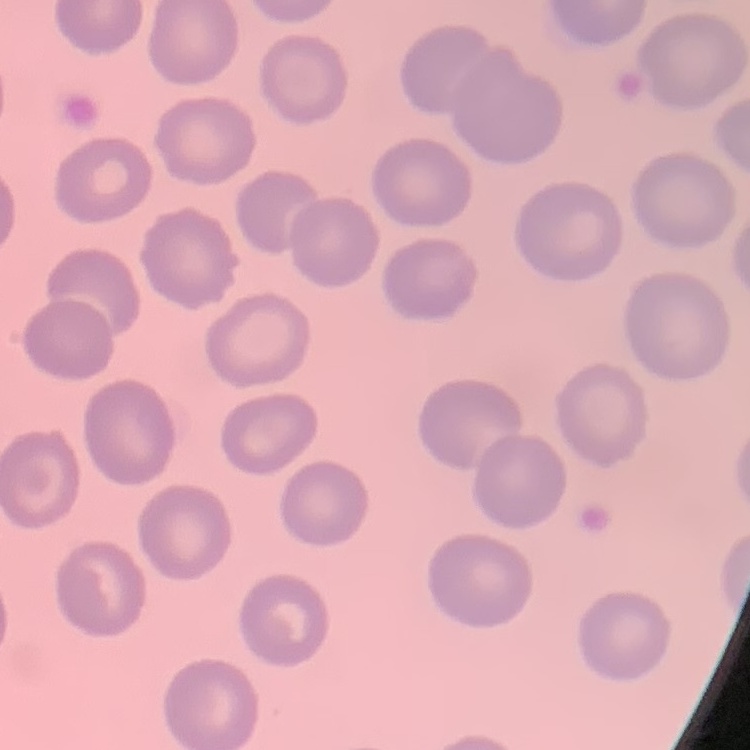 The erythrocytes exhibit no rouleaux formation. Thin peripheral smear. Stained with either Field's or Giemsa. One tile cut from a larger photomicrograph.